Point out every malaria parasite.
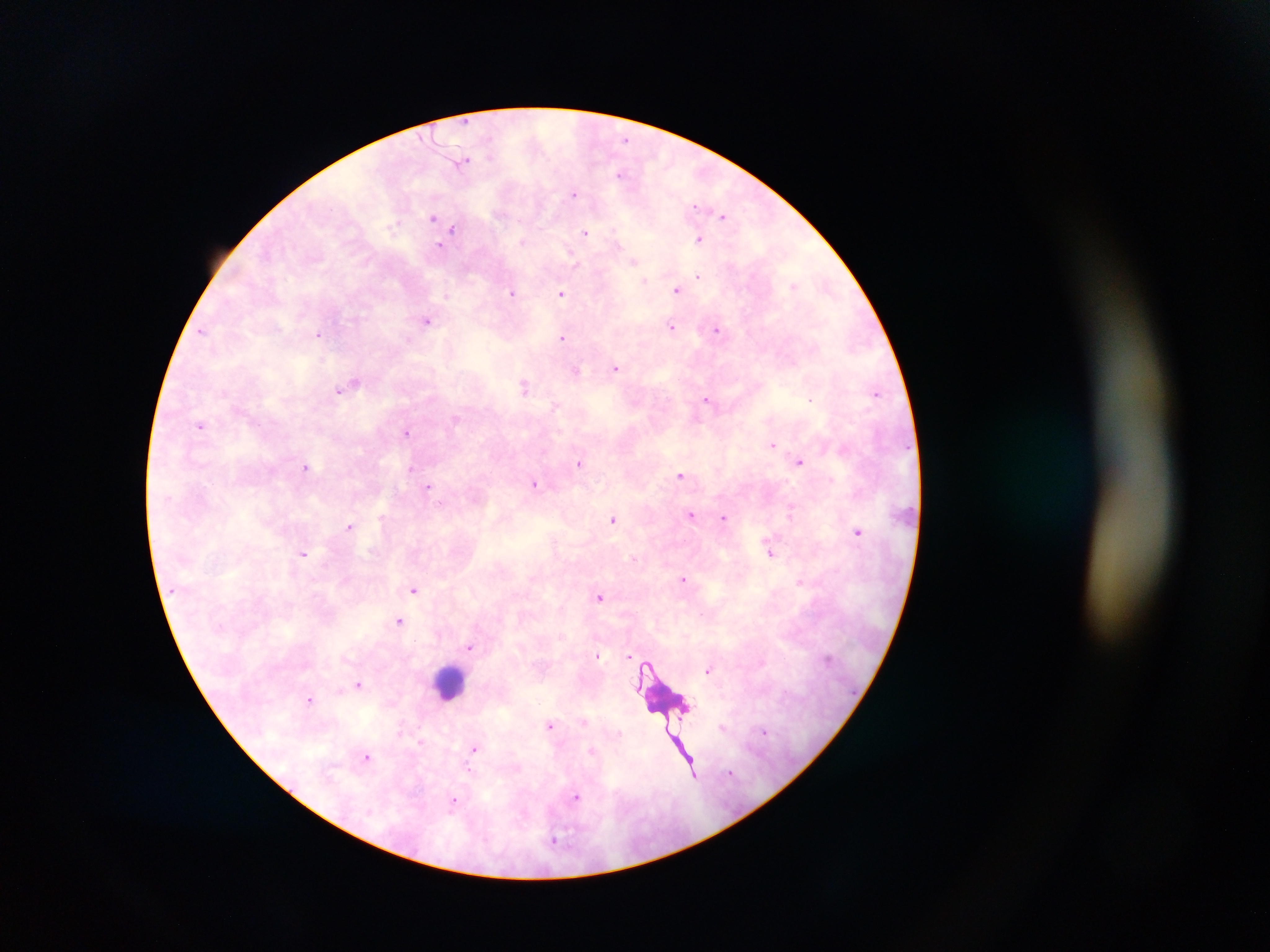

Approximate centers as (x, y) in pixels.
Malaria parasites: (463, 161), (623, 174), (575, 192), (695, 205), (724, 216), (434, 217), (453, 229), (585, 233), (700, 238), (635, 260), (698, 276), (795, 286), (678, 288), (561, 292), (514, 293), (427, 320), (672, 326), (719, 329), (202, 330), (320, 334), (563, 337), (616, 368), (576, 371), (354, 382), (525, 385), (347, 387), (338, 391), (876, 392), (812, 399), (708, 400), (201, 425), (407, 432), (772, 445), (801, 461), (579, 463), (307, 467), (412, 467), (680, 476), (536, 483), (429, 487), (792, 511), (691, 515), (724, 518), (614, 520), (350, 526), (858, 531), (771, 550), (303, 554), (634, 559), (685, 578), (800, 582), (414, 589), (600, 597), (400, 621), (470, 647), (597, 654), (630, 655), (709, 670), (359, 683), (310, 699), (552, 726), (723, 727), (766, 731), (421, 742), (475, 748), (592, 752), (367, 756), (694, 774), (577, 797), (455, 800).

Summary:
  - Leukocyte locations: (451, 683), (664, 703)
  - Image size: 1270×952 pixels
  - Capture: mobile-phone photograph through a microscope
  - Preparation: thick blood smear
  - Country: Ghana
  - Field of view: single